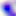
Summary:
  - Magnification: 400x
  - Identification: Toxoplasma gondii
  - Modality: photomicrograph